Describe the morphology of the erythrocytes.
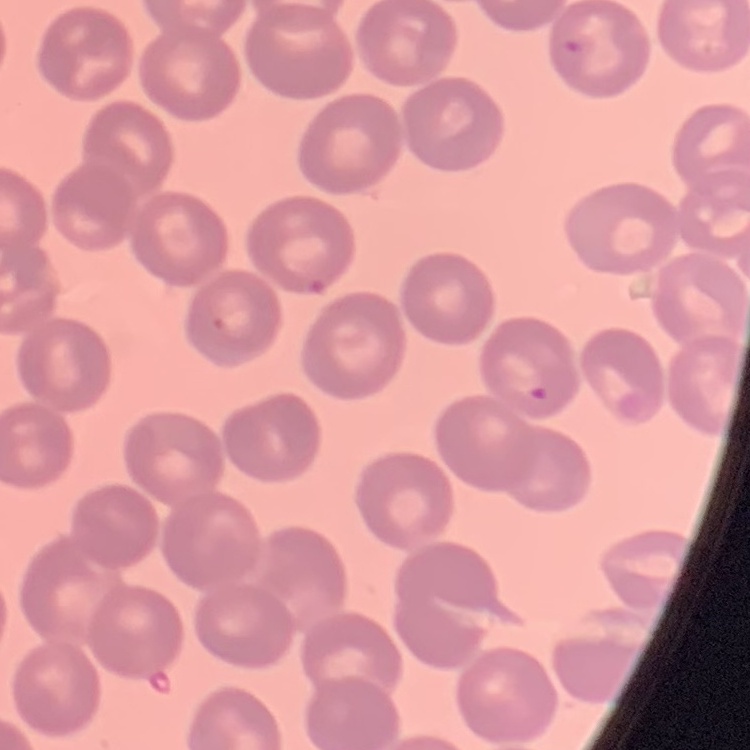

They show no rouleaux formation.

preparation = thin blood film
stain = Field's or Giemsa
image type = square crop of a larger photomicrograph